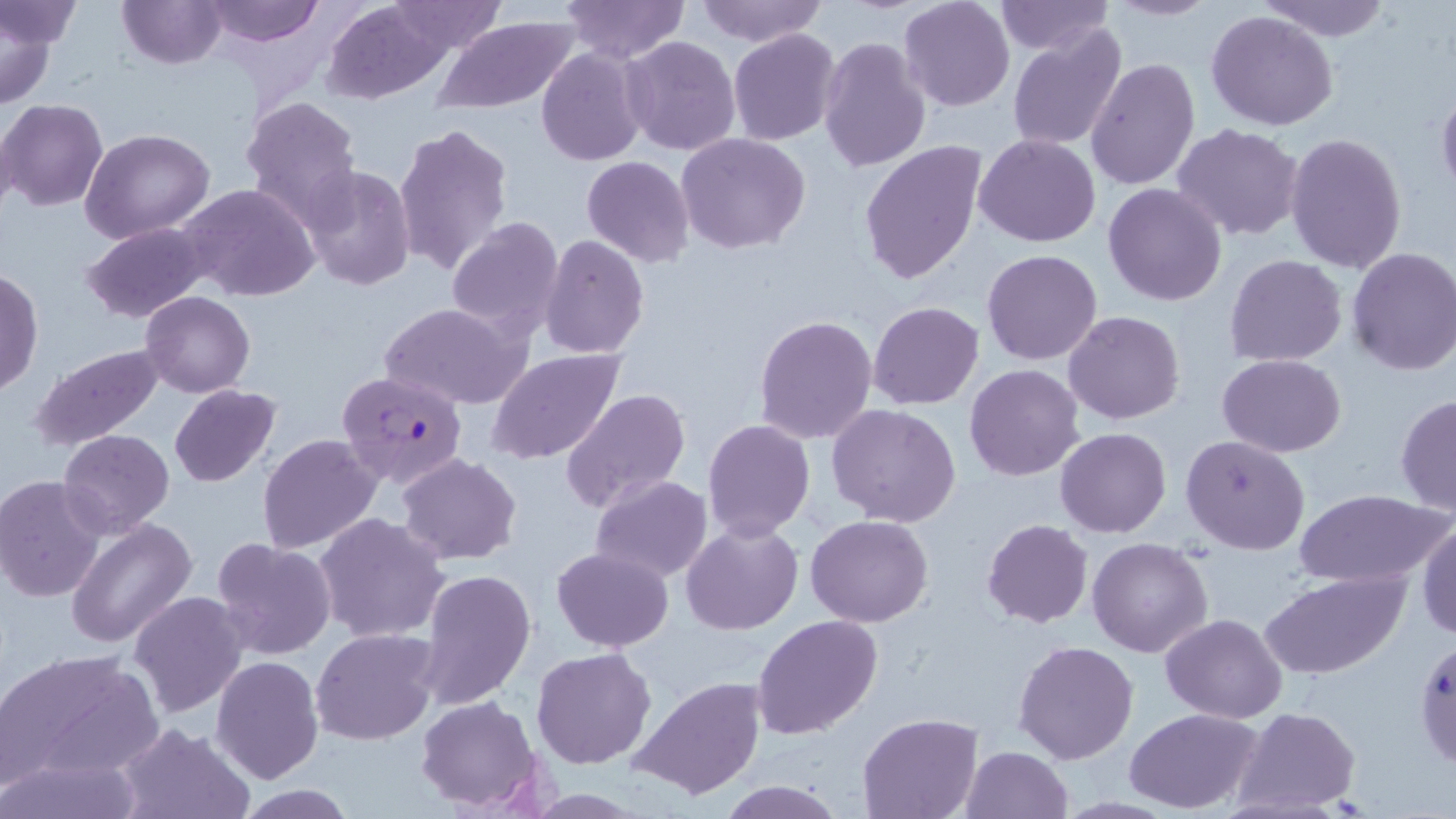
Approximate bounding boxes as [x1, y1, x2, y2] in pixels. Uninfected red blood cell locations: [0, 0, 83, 55], [117, 0, 227, 70], [206, 0, 324, 48], [561, 0, 689, 64], [693, 0, 826, 46], [898, 0, 1015, 111], [1104, 0, 1220, 22], [1254, 0, 1394, 41], [321, 1, 454, 103], [385, 1, 508, 54], [994, 1, 1112, 55], [1, 6, 61, 111], [1207, 9, 1339, 131], [432, 14, 578, 115], [1006, 23, 1127, 154], [728, 29, 842, 145], [622, 36, 741, 156], [819, 36, 930, 174], [536, 47, 647, 166], [1086, 58, 1200, 190], [1436, 79, 1456, 199], [241, 95, 363, 223], [1, 99, 107, 210], [393, 123, 512, 277], [1173, 123, 1305, 242], [81, 129, 214, 245], [1284, 131, 1407, 274], [676, 132, 810, 254], [973, 133, 1100, 247], [859, 141, 988, 286], [582, 155, 694, 267], [299, 164, 417, 293], [180, 183, 320, 302], [1103, 183, 1228, 306], [446, 216, 565, 341], [80, 222, 213, 325], [539, 234, 649, 359], [1345, 246, 1456, 377], [982, 249, 1103, 365], [1224, 253, 1348, 367], [1, 267, 43, 399], [140, 291, 255, 397], [868, 301, 985, 411], [382, 302, 528, 409], [1064, 311, 1184, 424], [753, 314, 877, 445], [29, 344, 166, 452], [486, 349, 627, 463], [1218, 354, 1347, 455], [964, 364, 1085, 481], [169, 385, 281, 486], [561, 388, 691, 513], [1395, 395, 1456, 516], [827, 403, 962, 528], [702, 418, 815, 540], [58, 428, 176, 536], [1053, 428, 1171, 538], [258, 434, 381, 554], [1181, 435, 1310, 556], [397, 453, 523, 565], [0, 475, 107, 602], [589, 475, 712, 583], [1295, 488, 1449, 588], [315, 512, 450, 644], [806, 515, 934, 626], [67, 518, 198, 648], [982, 519, 1094, 629], [680, 520, 802, 635], [1417, 520, 1456, 639], [208, 536, 336, 660], [1088, 536, 1214, 657], [551, 547, 673, 651], [418, 568, 535, 710], [1260, 570, 1411, 679], [129, 590, 249, 717], [1160, 612, 1288, 723], [754, 613, 883, 740], [312, 628, 440, 746], [1414, 637, 1456, 769], [1013, 640, 1139, 763], [530, 646, 657, 769], [1, 648, 163, 788], [210, 656, 323, 785], [628, 676, 768, 801], [412, 695, 546, 809], [1234, 706, 1361, 812], [1125, 708, 1263, 814], [858, 712, 982, 818], [113, 722, 253, 819], [960, 746, 1074, 819], [3, 750, 146, 819], [715, 780, 844, 817], [234, 786, 358, 818]. Plasmodium falciparum-infected red blood cell locations: [336, 368, 469, 489]. Slide-level diagnosis: Plasmodium falciparum. Optical microscopy. Captured at 1000x magnification. Single field of view. May-Grünwald-Giemsa-stained preparation. Thin blood film. Image is 1456×819 pixels.